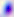

Summary:
  - Magnification: 400x
  - Identification: Toxoplasma gondii
  - Modality: photomicrograph